Assess this cell for malaria.
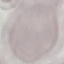
Uninfected.

Summary:
  - Preparation: thin smear
  - Stain: Giemsa
  - Image type: cell patch, automatically extracted from a larger field of view and resized to 64 × 64 pixels
  - Capture: smartphone camera at the microscope eyepiece